Name the parasite shown.
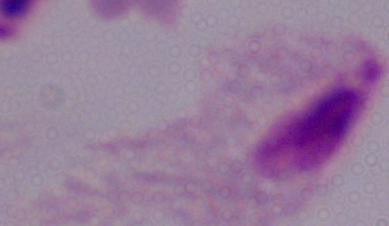
This is a trichomonad.

Photomicrograph. 1000x magnification.